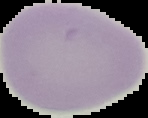

Summary:
  - Preparation: thin blood film
  - Image type: segmented cell region with the area outside set to black
  - Image size: 148×118 pixels
  - Result: no malaria parasites seen